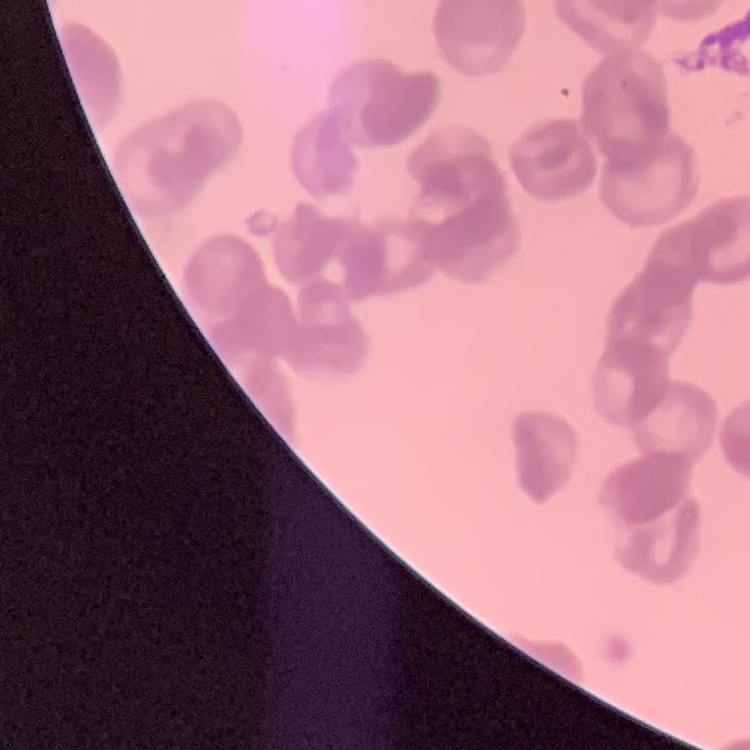

Summary:
  - Erythrocyte morphology: rouleaux formation
  - Image type: one tile cut from a larger photomicrograph
  - Stain: Field's or Giemsa
  - Preparation: thin blood film